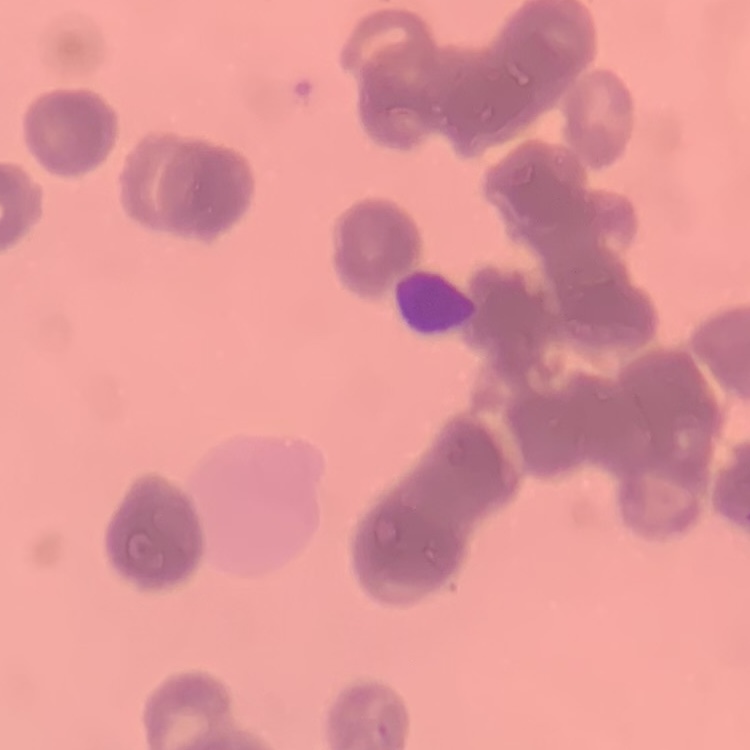

The erythrocytes show rouleaux formation. Field's or Giemsa stain. One tile cut from a larger photomicrograph. Thin blood smear.